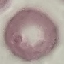

Result: negative for malaria parasites. Cell patch, automatically extracted from a larger field of view and resized to 64 × 64 pixels. Acquired by smartphone through the microscope eyepiece. Thin blood film. Giemsa-stained preparation.